Name the blood parasite species.
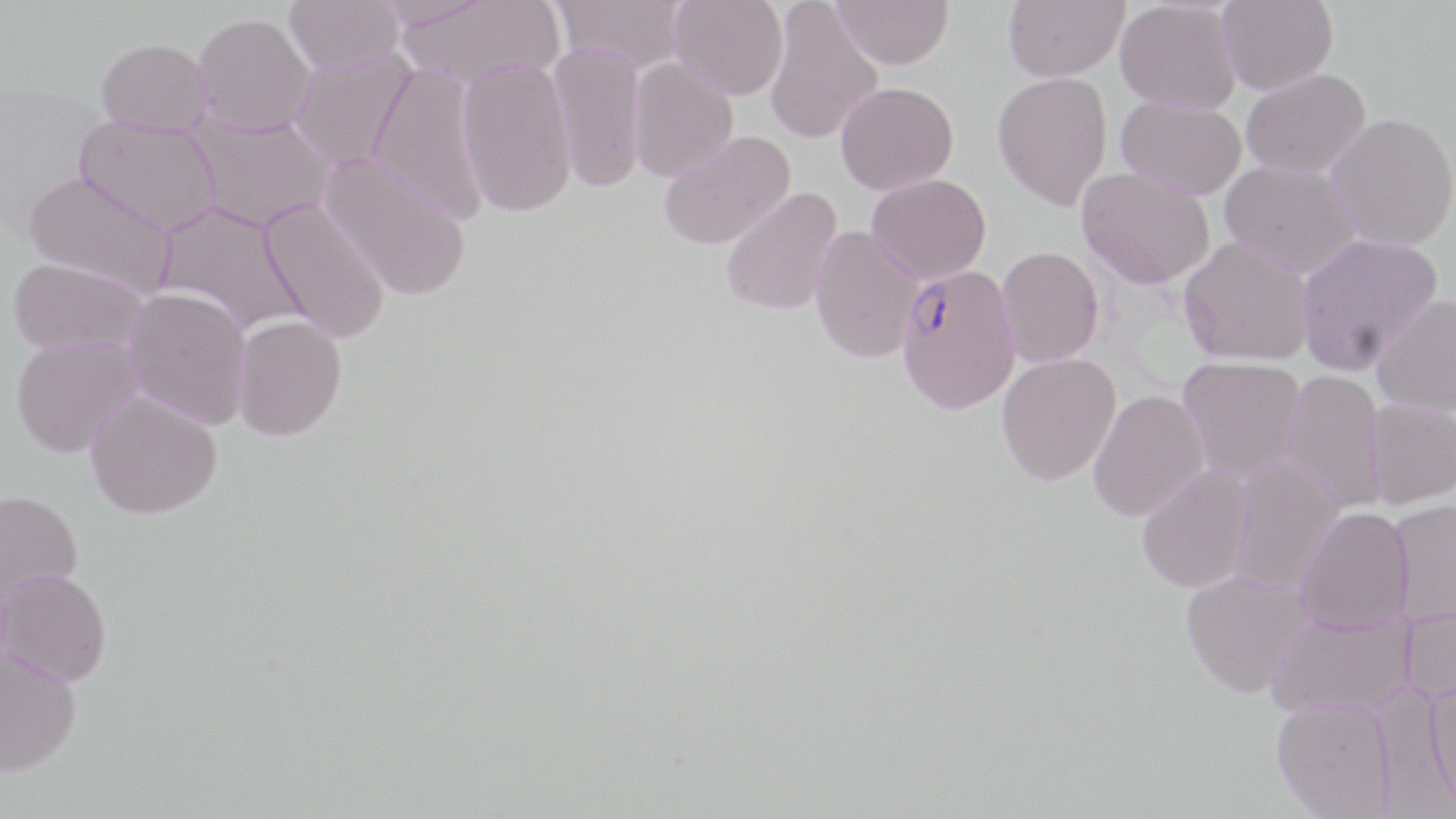

Plasmodium falciparum.

{
  "preparation": "thin blood film",
  "image_size": "1456×819 pixels",
  "modality": "optical microscopy",
  "stain": "May-Grünwald-Giemsa",
  "field_of_view": "single",
  "uninfected_red_blood_cell_locations": "approximate bounding boxes as (x1, y1, x2, y2) in pixels: (284, 0, 403, 75), (395, 0, 565, 91), (551, 0, 688, 74), (668, 0, 789, 101), (831, 0, 954, 70), (1003, 0, 1129, 83), (1217, 0, 1338, 94), (1115, 1, 1242, 114), (764, 2, 884, 145), (193, 13, 314, 137), (96, 38, 212, 137), (548, 40, 647, 194), (290, 47, 416, 172), (456, 57, 577, 218), (628, 57, 738, 182), (369, 62, 489, 225), (1241, 68, 1371, 179), (992, 71, 1112, 210), (835, 81, 959, 194), (1116, 96, 1246, 201), (187, 109, 335, 233), (1325, 112, 1456, 251), (75, 116, 220, 235), (657, 130, 796, 250), (319, 151, 472, 301), (1219, 161, 1362, 279), (1076, 167, 1214, 289), (23, 171, 176, 297), (866, 173, 991, 285), (719, 187, 844, 316), (259, 198, 391, 343), (154, 201, 306, 336), (810, 225, 924, 363), (1295, 233, 1444, 376), (1178, 237, 1316, 366), (995, 246, 1104, 368), (7, 257, 148, 355), (123, 286, 252, 429), (1371, 295, 1456, 419), (232, 314, 347, 442), (9, 334, 144, 458), (996, 352, 1121, 486), (1176, 356, 1307, 485), (1282, 369, 1385, 514), (84, 389, 222, 519), (1088, 390, 1210, 522), (1365, 399, 1456, 509), (1224, 454, 1347, 598), (1136, 464, 1254, 593), (0, 490, 84, 608), (1388, 500, 1456, 627), (1294, 506, 1415, 633), (0, 569, 112, 687), (1180, 570, 1314, 698), (1400, 599, 1456, 706), (1264, 609, 1415, 719), (0, 644, 81, 775), (1425, 677, 1456, 810), (1271, 698, 1396, 818)",
  "magnification": "1000x",
  "plasmodium_falciparum_infected_red_blood_cell_locations": "approximate bounding boxes as (x1, y1, x2, y2) in pixels: (894, 264, 1022, 415)"
}